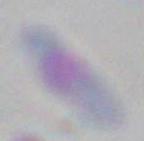

Summary:
  - Magnification: 1000x
  - Identification: Toxoplasma gondii
  - Modality: micrograph